Give the position of every Plasmodium parasite.
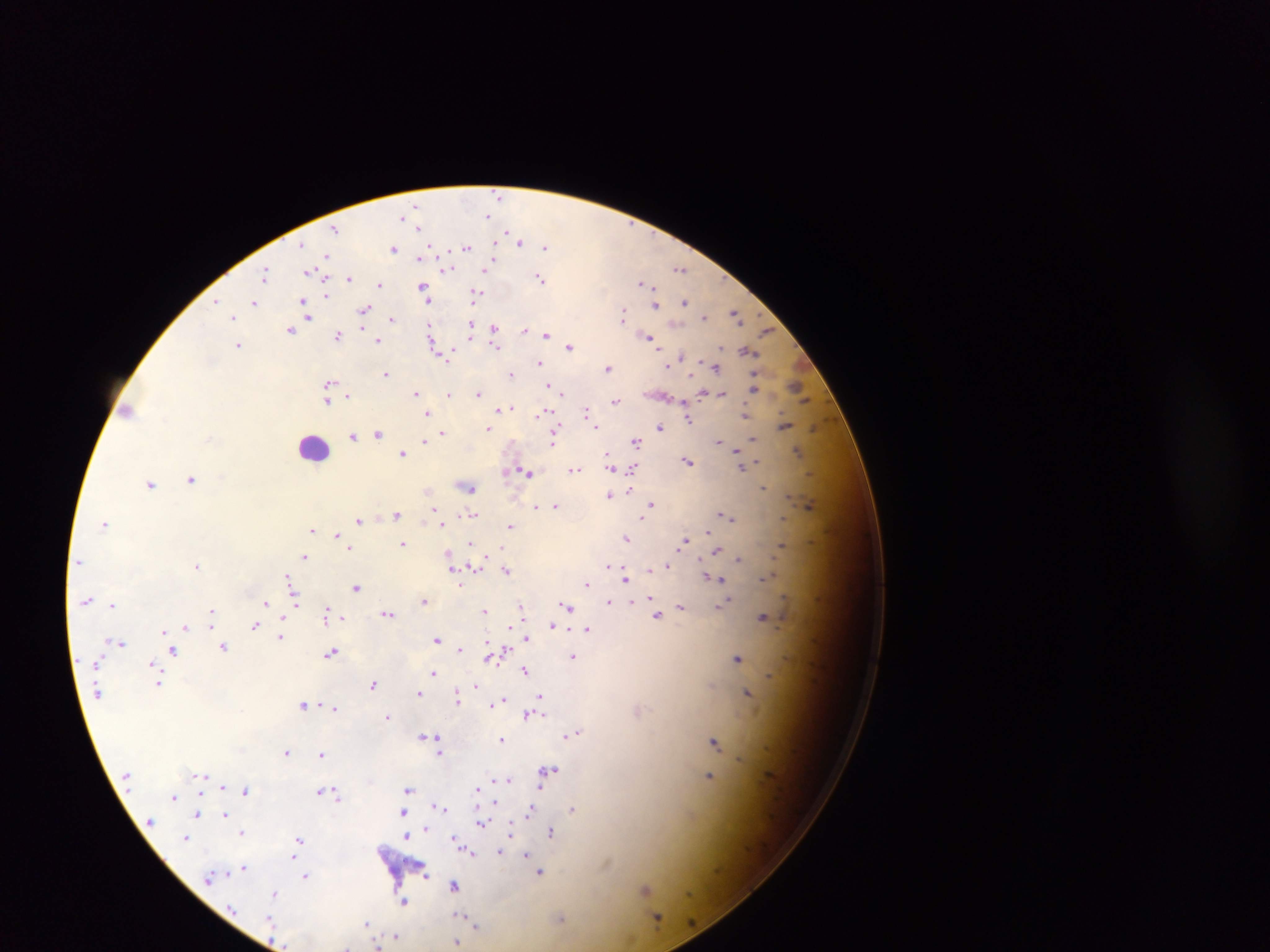
Approximate centers as x y in pixels.
Plasmodium parasites: 500 195; 416 207; 488 217; 403 219; 412 219; 419 226; 335 229; 520 240; 466 247; 545 247; 393 249; 420 257; 328 258; 492 262; 447 268; 487 268; 680 269; 311 271; 266 273; 319 276; 541 276; 350 278; 643 282; 380 284; 425 292; 475 293; 216 301; 254 302; 685 302; 656 305; 306 307; 365 308; 736 312; 308 314; 623 314; 233 317; 704 317; 393 319; 430 327; 473 327; 290 329; 362 329; 495 329; 525 329; 532 330; 767 331; 545 333; 338 334; 649 338; 432 339; 378 340; 238 345; 497 346; 570 346; 440 349; 748 351; 449 352; 681 356; 540 362; 672 362; 716 366; 609 367; 386 373; 512 374; 329 384; 798 386; 553 387; 754 387; 479 391; 417 392; 562 392; 702 392; 328 393; 449 393; 710 393; 721 393; 346 395; 328 399; 615 401; 508 407; 501 408; 128 409; 587 410; 544 411; 428 413; 745 414; 688 417; 784 425; 596 426; 660 427; 488 428; 557 428; 816 428; 379 432; 442 433; 353 435; 554 435; 752 438; 719 439; 425 441; 636 441; 742 449; 798 450; 403 452; 738 453; 608 456; 689 460; 757 462; 611 463; 741 465; 634 467; 574 469; 526 471; 506 472; 192 479; 151 484; 467 486; 764 488; 630 489; 609 494; 651 503; 556 505; 810 505; 535 506; 397 513; 434 513; 473 514; 722 515; 728 516; 644 518; 360 519; 783 521; 441 522; 105 524; 511 525; 313 530; 708 531; 337 534; 627 538; 685 540; 403 543; 471 544; 782 544; 351 549; 717 550; 450 552; 305 556; 451 557; 738 559; 196 565; 608 566; 667 566; 472 567; 454 568; 617 568; 651 568; 506 570; 625 577; 291 578; 713 578; 764 578; 587 583; 356 587; 652 598; 423 600; 631 600; 609 601; 266 603; 295 603; 723 604; 113 605; 681 606; 522 607; 568 607; 485 610; 211 611; 327 613; 388 613; 658 615; 763 617; 212 619; 255 625; 511 626; 552 626; 187 628; 588 628; 164 630; 526 636; 281 638; 437 640; 122 643; 224 646; 460 649; 173 650; 499 652; 332 653; 493 656; 574 656; 738 658; 152 663; 434 670; 525 670; 769 676; 160 683; 373 683; 475 685; 711 686; 419 694; 747 694; 541 695; 458 698; 503 700; 304 703; 494 703; 322 704; 309 706; 335 709; 529 714; 388 716; 571 734; 424 736; 439 739; 503 740; 714 741; 439 745; 287 752; 439 752; 322 754; 740 759; 549 770; 202 774; 710 776; 499 780; 509 780; 540 787; 479 788; 409 789; 245 790; 321 790; 336 794; 175 797; 494 803; 439 806; 531 809; 573 809; 404 812; 197 813; 225 813; 481 823; 425 828; 242 831; 513 831; 553 831; 410 832; 407 835; 187 837; 299 838; 456 838; 472 852; 501 853; 526 854; 295 855; 531 860; 243 867; 540 872; 427 874; 306 876; 455 885; 645 890; 275 892; 404 902; 461 916; 657 916; 270 917; 560 918; 470 921; 368 923; 475 925; 395 935; 456 941; 377 945; 345 946.

Summary:
  - Leukocyte locations: 313 447
  - Capture: mobile-phone photograph through a microscope
  - Preparation: thick blood smear
  - Image size: 1270×952 pixels
  - Field of view: single
  - Country: Ghana